Assess this cell for malaria.
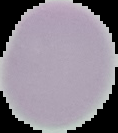

Uninfected.

{
  "preparation": "thin blood smear",
  "image_type": "segmented cell region with the area outside set to black",
  "image_size": "118×133 pixels"
}